State the blood parasite species.
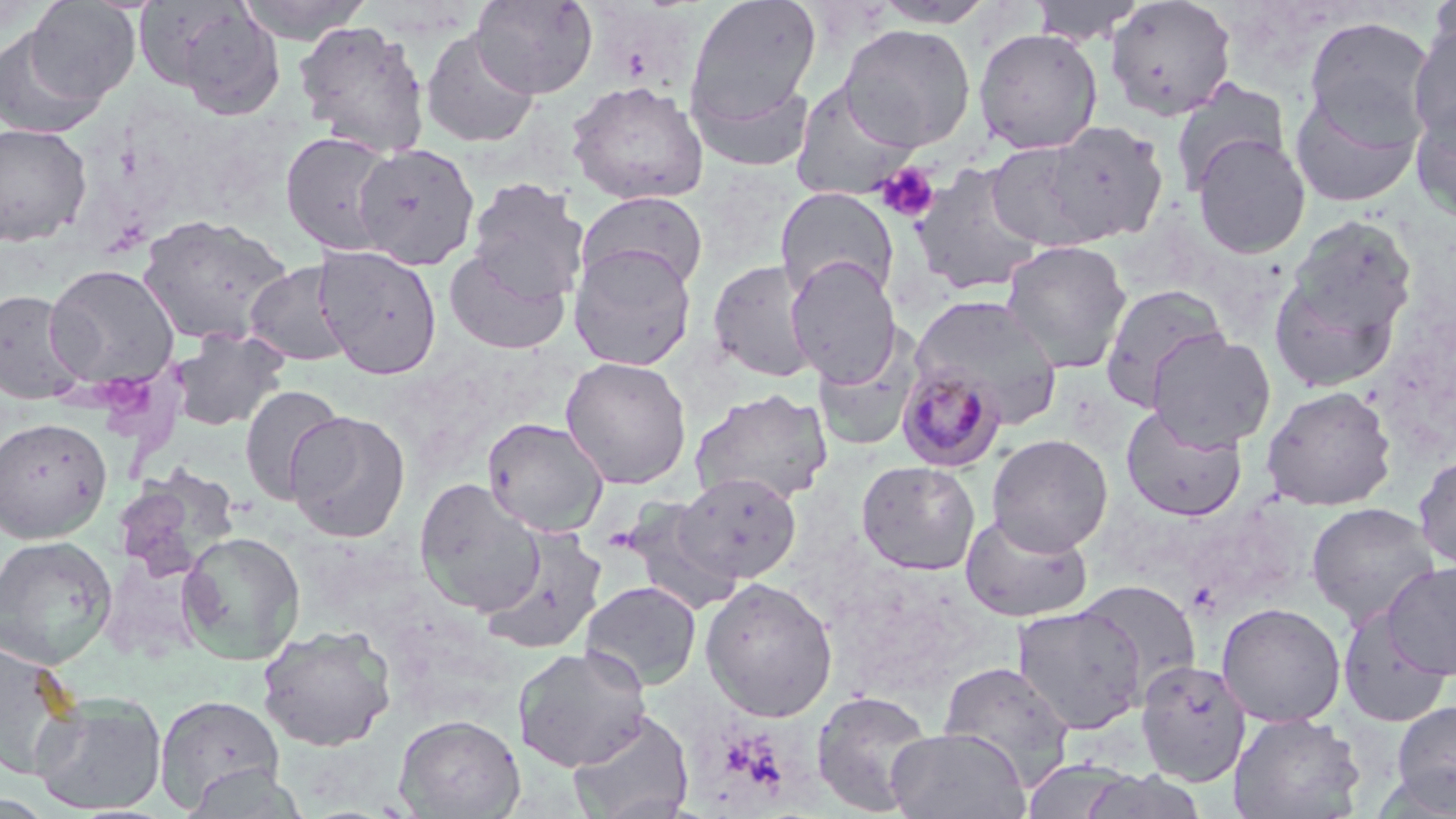

Plasmodium malariae.

platelet locations = approximate bounding boxes as [x1, y1, x2, y2] in pixels: [875, 163, 940, 223], [98, 375, 162, 426]
modality = optical microscopy
field of view = one of a larger specimen
image size = 1456×819 pixels
preparation = thin blood smear
magnification = 1000x
uninfected red blood cell locations = approximate bounding boxes as [x1, y1, x2, y2] in pixels: [236, 0, 373, 43], [470, 0, 599, 99], [685, 0, 822, 126], [869, 0, 996, 28], [1029, 0, 1147, 46], [1425, 0, 1456, 70], [25, 1, 141, 104], [1104, 1, 1237, 121], [154, 2, 287, 119], [1302, 15, 1439, 142], [293, 20, 431, 156], [1408, 20, 1456, 143], [839, 23, 977, 152], [0, 26, 108, 141], [972, 27, 1104, 155], [420, 28, 540, 149], [688, 72, 816, 173], [1169, 78, 1291, 195], [565, 80, 709, 206], [789, 80, 920, 201], [1289, 88, 1422, 208], [1410, 97, 1456, 223], [1037, 120, 1169, 245], [0, 122, 93, 247], [279, 130, 399, 256], [1191, 133, 1311, 259], [984, 139, 1107, 251], [352, 144, 480, 270], [910, 161, 1047, 296], [466, 177, 590, 300], [775, 187, 899, 303], [577, 190, 709, 293], [137, 214, 293, 347], [1281, 215, 1418, 356], [1000, 239, 1133, 374], [313, 244, 443, 380], [568, 244, 697, 371], [444, 248, 571, 356], [786, 257, 901, 384], [707, 259, 818, 383], [244, 261, 355, 368], [1265, 261, 1406, 396], [44, 263, 180, 389], [1099, 283, 1231, 408], [0, 288, 87, 405], [910, 294, 1064, 425], [168, 327, 290, 433], [1146, 330, 1276, 450], [812, 331, 921, 453], [560, 356, 692, 490], [238, 384, 345, 504], [1261, 385, 1398, 511], [689, 388, 833, 506], [1121, 404, 1248, 520], [286, 410, 410, 543], [0, 416, 113, 543], [481, 417, 610, 537], [986, 433, 1113, 555], [1413, 451, 1456, 572], [854, 455, 1112, 568], [856, 460, 981, 575], [116, 467, 241, 582], [677, 472, 802, 583], [414, 477, 545, 617], [619, 501, 745, 612], [1306, 501, 1441, 629], [959, 511, 1093, 623], [479, 527, 607, 657], [177, 531, 306, 664], [0, 534, 119, 670], [1382, 560, 1456, 681], [699, 576, 838, 722], [1077, 579, 1201, 698], [581, 580, 702, 690], [1216, 602, 1346, 727], [1012, 604, 1147, 734], [1336, 608, 1453, 728], [257, 624, 397, 751], [0, 636, 82, 779], [512, 644, 652, 772], [1135, 658, 1251, 785], [936, 660, 1076, 788], [811, 689, 936, 816], [30, 692, 168, 816], [154, 694, 285, 812], [1390, 699, 1456, 812], [566, 709, 695, 819], [1229, 711, 1366, 819], [394, 713, 524, 818], [886, 727, 1030, 819], [182, 763, 310, 818]
stain = May-Grünwald-Giemsa
Plasmodium malariae-infected red blood cell locations = approximate bounding boxes as [x1, y1, x2, y2] in pixels: [896, 362, 1008, 473]